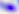
Summary:
  - Identification: Toxoplasma gondii
  - Magnification: 400x
  - Modality: photomicrograph